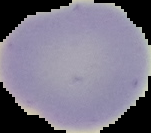

Segmented cell region on a black background. Image is 151×133 pixels. From a thin blood film. Malaria status: uninfected.